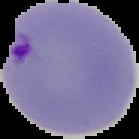
{
  "malaria_status": "parasitized",
  "preparation": "thin blood smear",
  "image_size": "139×139 pixels",
  "image_type": "cell region segmented out of the field of view; surrounding area masked to black"
}